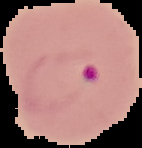 From a thin blood smear. Image is 142×148 pixels. Malaria status: parasitized. The area outside the segmented cell region is set to black.